Classify this cell by malaria status.
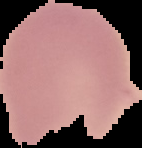
It is uninfected.

preparation = thin blood film
image type = segmented cell region on a black background
image size = 142×148 pixels